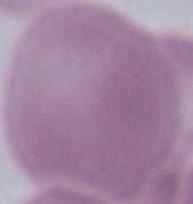
An erythrocyte is shown. Photomicrograph. 1000x magnification.